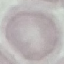
Summary:
  - Result: no malaria parasites detected
  - Preparation: thin blood smear
  - Stain: Giemsa
  - Image type: automatically extracted cell patch, resized to 64 × 64 pixels
  - Capture: smartphone camera at the microscope eyepiece